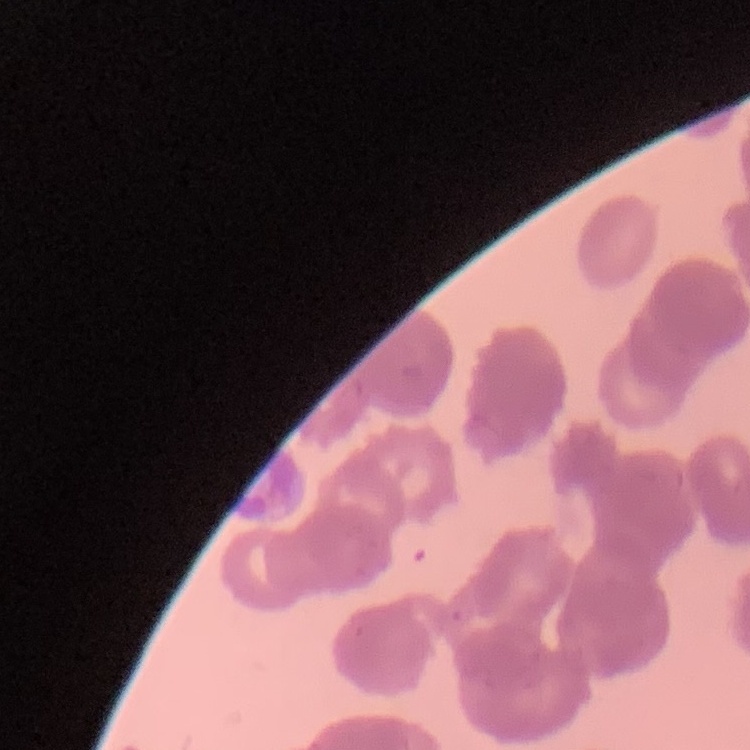

Summary:
  - Red blood cell morphology: rouleaux formation
  - Stain: Field's or Giemsa
  - Preparation: thin blood film
  - Image type: one tile cut from a larger photomicrograph